Report the malaria status of this cell.
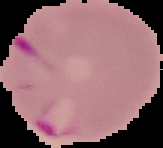

Parasitized.

image_size: 163×148 pixels
preparation: thin blood film
image_type: segmented cell region with the area outside set to black